Name the parasite shown.
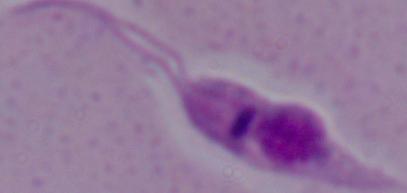
This is Leishmania.

{
  "modality": "micrograph",
  "magnification": "1000x"
}